Report the malaria status of this cell.
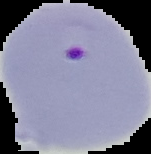

Parasitized.

Summary:
  - Image size: 151×154 pixels
  - Image type: segmented cell region on a black background
  - Preparation: thin blood film